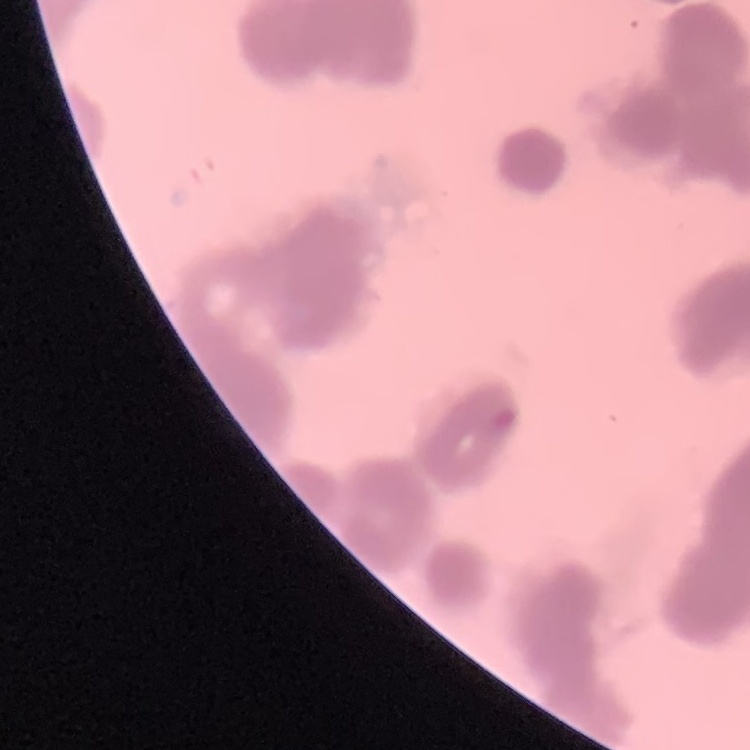
red_blood_cell_morphology: rouleaux formation
image_type: one tile cut from a larger photomicrograph
stain: Field's or Giemsa
preparation: thin blood film